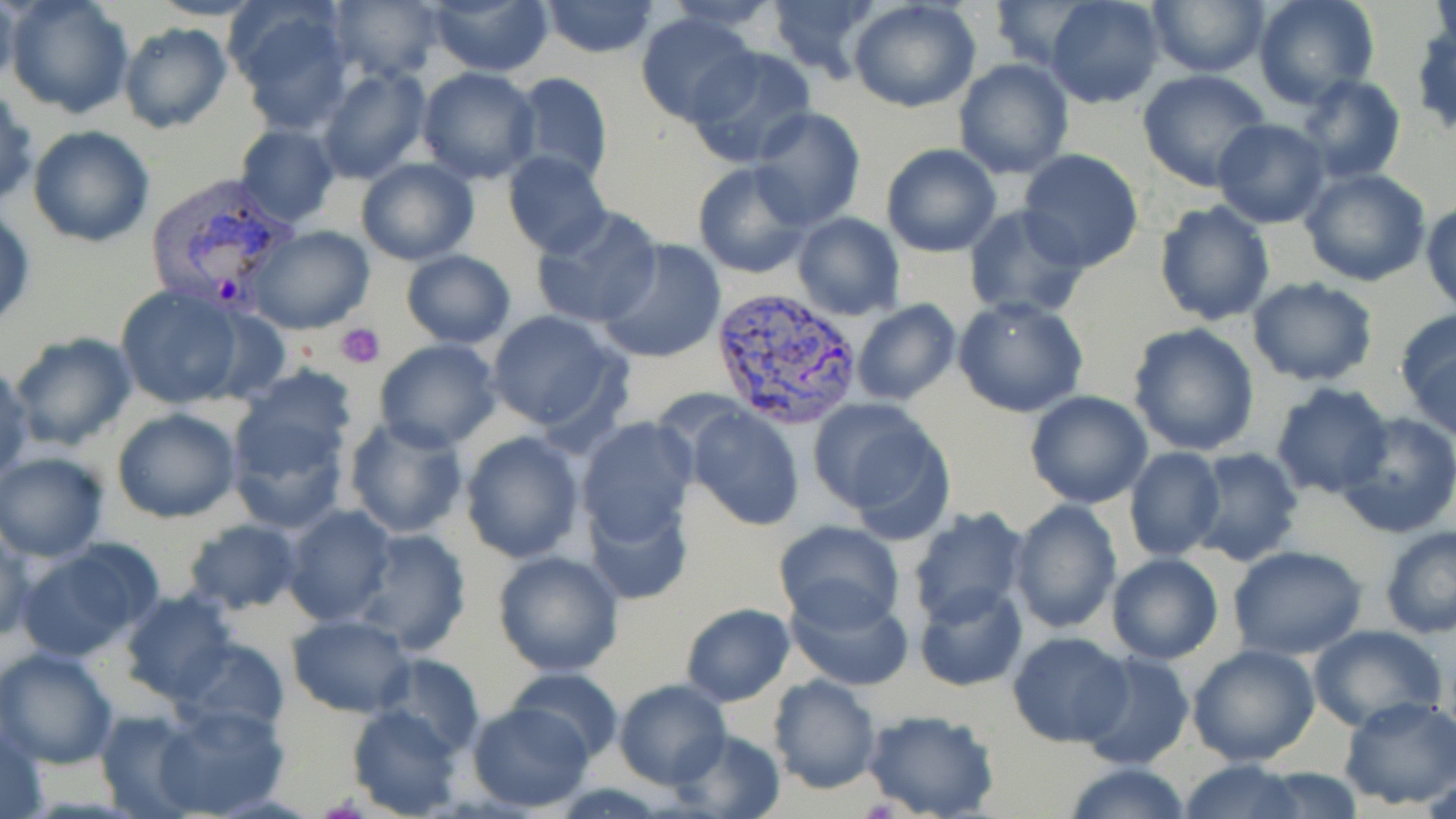
Summary:
  - Coordinate format: approximate bounding boxes as (x1, y1, x2, y2) in pixels
  - Plasmodium vivax-infected red blood cell locations: (143, 171, 302, 318), (711, 286, 864, 430)
  - Uninfected red blood cell locations: (0, 0, 18, 90), (5, 0, 136, 120), (149, 0, 263, 21), (328, 0, 443, 82), (426, 0, 555, 75), (538, 0, 660, 57), (668, 0, 785, 34), (766, 0, 883, 82), (1045, 0, 1166, 107), (1147, 0, 1270, 77), (1251, 0, 1380, 109), (227, 1, 356, 130), (847, 1, 983, 113), (989, 1, 1101, 72), (635, 13, 759, 124), (870, 15, 1027, 153), (117, 22, 231, 134), (684, 48, 817, 168), (953, 58, 1073, 180), (317, 66, 430, 183), (416, 67, 543, 185), (1137, 70, 1274, 193), (506, 73, 613, 190), (1296, 75, 1406, 184), (0, 84, 37, 211), (750, 107, 865, 229), (1211, 118, 1331, 228), (235, 124, 339, 226), (27, 125, 156, 248), (880, 144, 1002, 257), (1017, 150, 1144, 274), (502, 151, 612, 258), (357, 158, 478, 266), (692, 162, 815, 278), (1299, 167, 1432, 286), (1152, 200, 1276, 325), (1423, 203, 1456, 313), (961, 205, 1092, 321), (530, 206, 662, 330), (791, 213, 906, 321), (249, 226, 374, 334), (596, 238, 726, 365), (400, 250, 516, 348), (1247, 276, 1380, 386), (113, 284, 248, 410), (952, 297, 1088, 418), (852, 299, 960, 406), (484, 309, 630, 438), (1394, 309, 1456, 439), (1127, 321, 1260, 455), (8, 331, 139, 452), (372, 339, 501, 452), (0, 362, 32, 482), (233, 364, 361, 478), (1269, 383, 1393, 498), (1024, 391, 1153, 509), (226, 396, 351, 532), (808, 399, 953, 534), (687, 405, 807, 531), (111, 408, 241, 523), (1334, 412, 1456, 538), (342, 414, 470, 539), (577, 419, 697, 542), (459, 430, 585, 561), (1190, 446, 1303, 565), (1124, 449, 1225, 561), (0, 452, 109, 561), (586, 491, 695, 605), (1008, 500, 1122, 634), (283, 504, 397, 626), (906, 507, 1030, 628), (182, 517, 303, 617), (772, 520, 906, 629), (0, 522, 32, 644), (1378, 525, 1456, 638), (349, 528, 472, 655), (15, 539, 161, 661), (1227, 546, 1369, 659), (491, 550, 625, 677), (1106, 554, 1223, 665), (782, 579, 915, 691), (914, 582, 1029, 692), (119, 591, 239, 705), (681, 603, 795, 707), (286, 614, 415, 716), (1306, 624, 1447, 734), (1007, 632, 1132, 746), (169, 636, 289, 737), (1187, 643, 1321, 767), (0, 646, 119, 769), (1076, 651, 1196, 771), (374, 654, 483, 756), (506, 667, 623, 761), (767, 674, 882, 795), (614, 679, 731, 788), (1336, 695, 1456, 809), (153, 702, 290, 816), (466, 702, 594, 812), (348, 705, 466, 816), (95, 708, 205, 817), (862, 709, 1001, 819), (1, 718, 49, 819), (666, 728, 784, 818), (1179, 759, 1309, 819), (1061, 763, 1196, 819), (1251, 766, 1365, 818)
  - Platelet locations: (336, 322, 385, 368)
  - Slide-level diagnosis: Plasmodium vivax
  - Field of view: single
  - Magnification: 1000x
  - Preparation: thin blood smear
  - Modality: optical microscopy
  - Stain: May-Grünwald-Giemsa
  - Image size: 1456×819 pixels